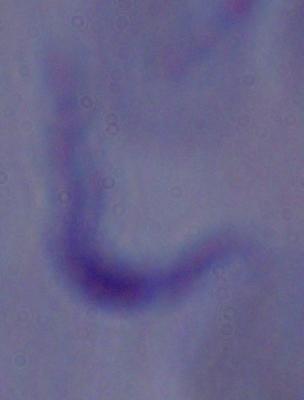

magnification = 1000x
modality = micrograph
identification = trypanosome